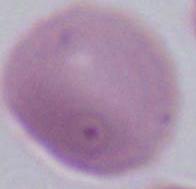 A red blood cell is shown. Photomicrograph. Captured at 1000x magnification.